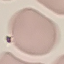

Summary:
  - Result: no malaria parasites seen
  - Capture: smartphone camera at the microscope eyepiece
  - Stain: Giemsa
  - Preparation: thin blood film
  - Image type: automatically extracted cell patch, resized to 64 × 64 pixels